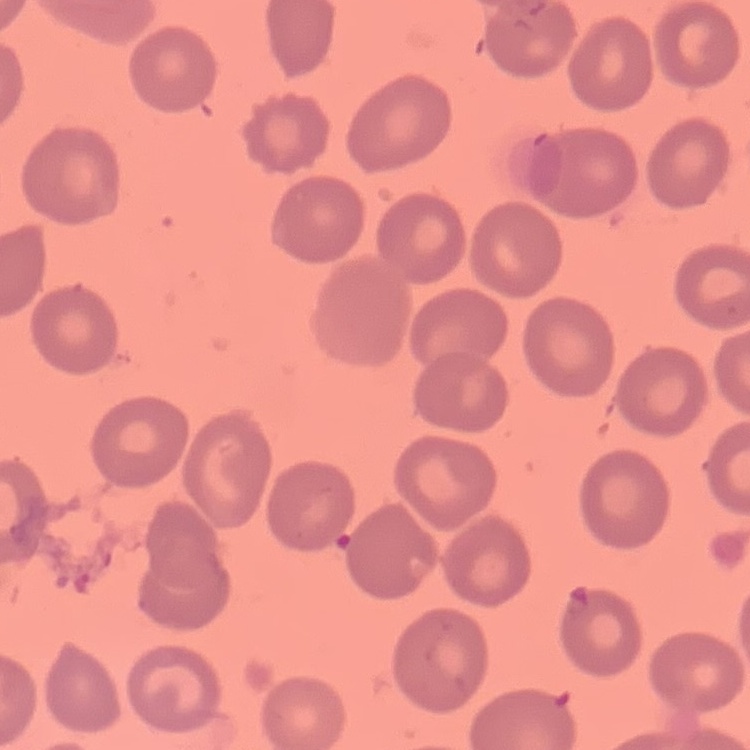
red_blood_cell_morphology: no rouleaux formation
preparation: thin blood smear
stain: Field's or Giemsa
image_type: square crop of a larger photomicrograph